Give the position of each Plasmodium falciparum parasite with its life-cycle stage, each leukocyte, and any debris.
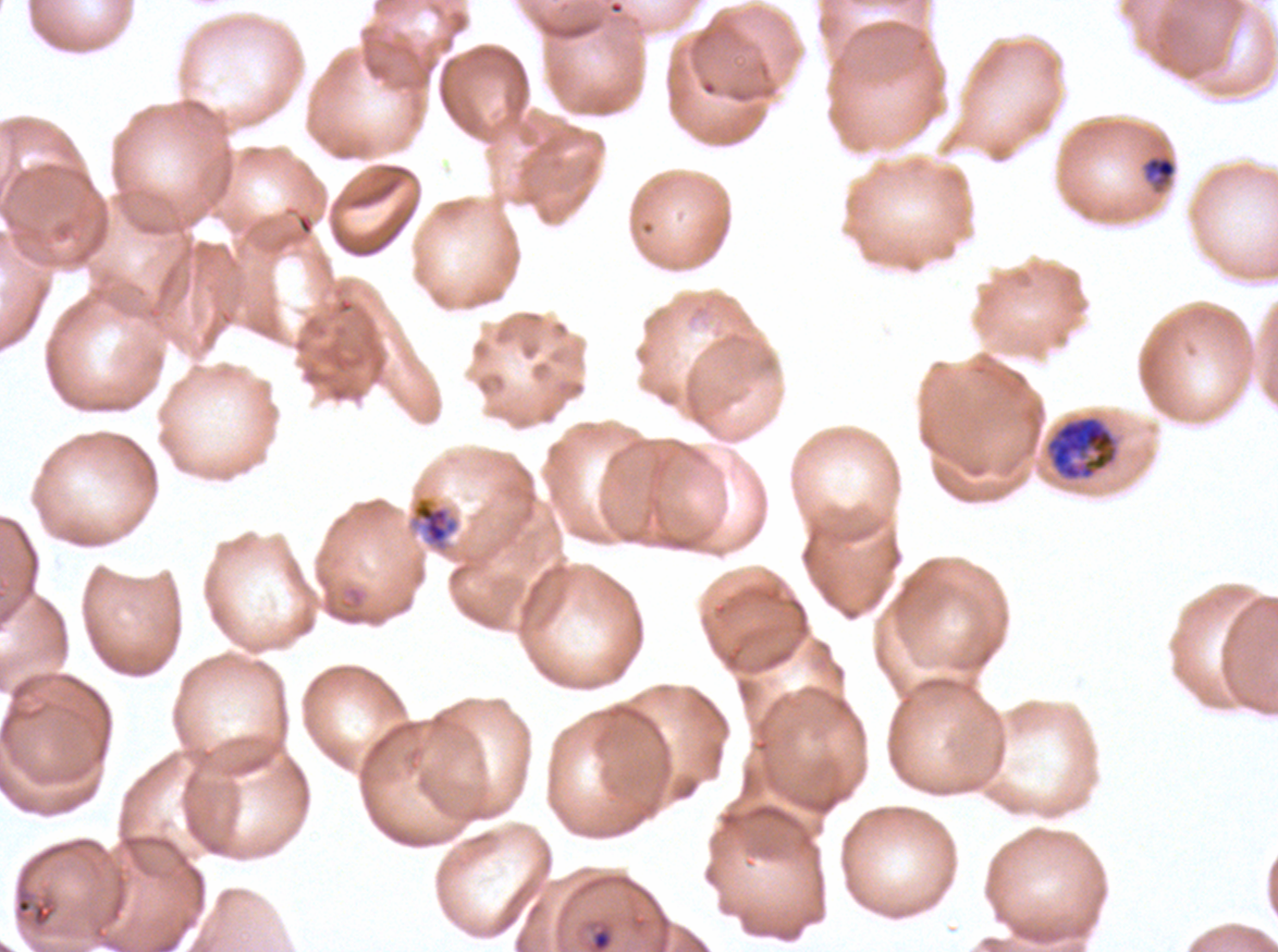

Approximate bounding boxes as (x1, y1, x2, y2) in pixels.
Rings: (591, 928, 612, 951).
Late-ring/early-trophozoite forms: (1142, 155, 1177, 188).
Mid trophozoites: (410, 495, 460, 553).
Early schizonts: (1046, 416, 1116, 480).
No late trophozoites, late schizonts, segmenters, gametocytes, leukocytes, or debris observed.

{
  "stain": "Giemsa",
  "preparation": "thin blood smear",
  "life_cycle_stages_observed": "ring, late-ring/early-trophozoite, mid trophozoite, early schizont",
  "field_of_view": "one sub-image of a larger composite",
  "specimen": "Plasmodium falciparum from a patient in The Gambia, cultured ex vivo for 24 to 48 hours",
  "image_size": "1278×952 pixels"
}